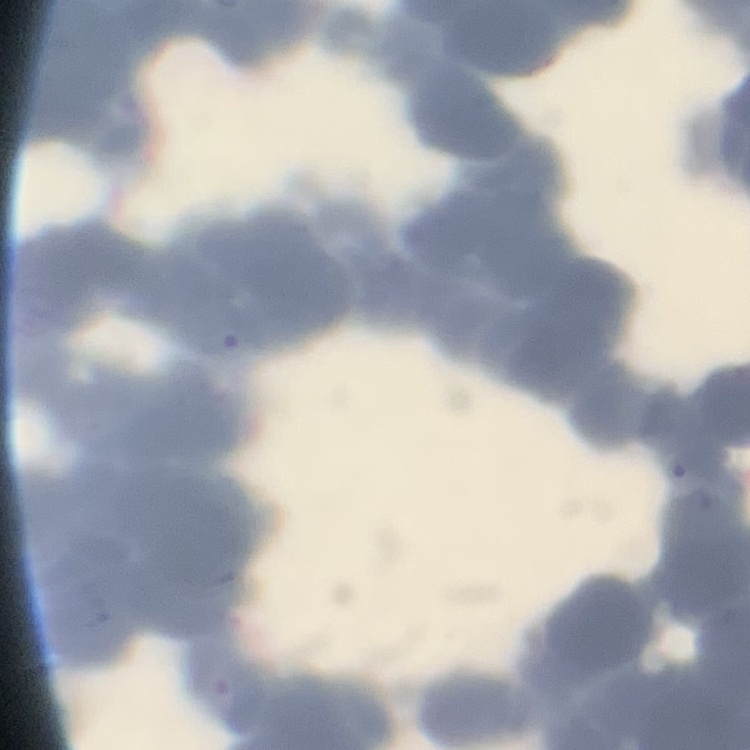
erythrocyte morphology = rouleaux formation
image type = square crop of a larger photomicrograph
preparation = thin blood film
stain = Field's or Giemsa